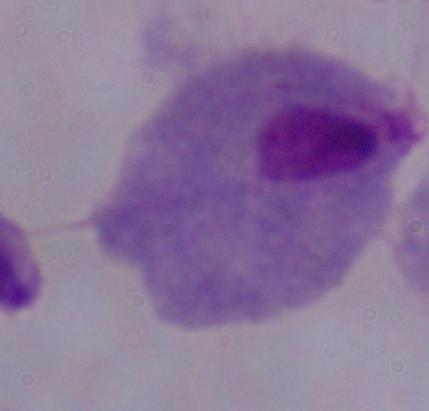
Photomicrograph. 1000x magnification. A trichomonad is seen.